Mark where leukocytes are.
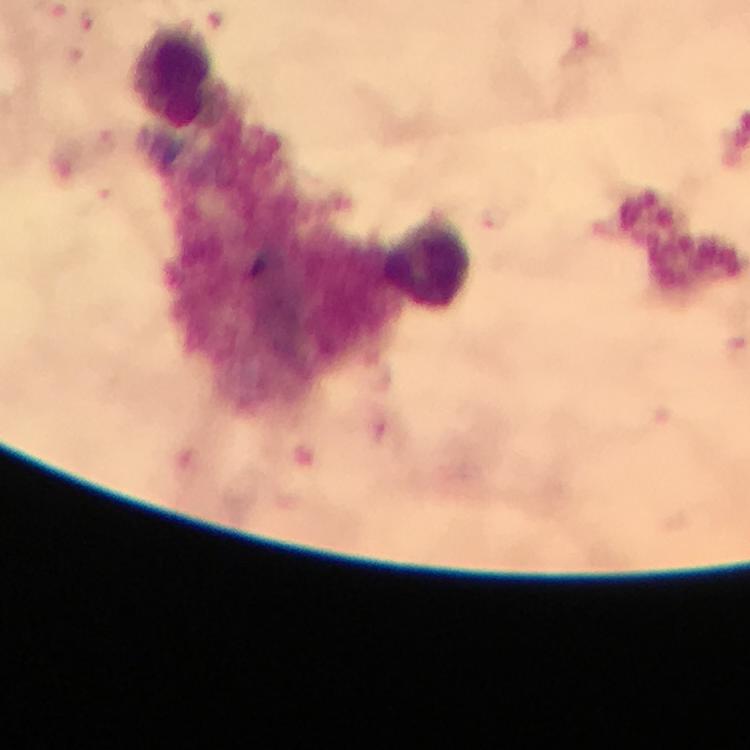

Approximate object centers, in pixels from the top-left corner.
Leukocytes: (x=171, y=74), (x=427, y=261).

Malaria parasite locations: (x=89, y=19), (x=107, y=145), (x=492, y=219). Immersion oil applied. Image is 750×750 pixels. Giemsa-stained preparation. From a malaria diagnostic workup. Thick blood smear. A crop from one field of view. Smartphone photograph taken through a microscope. At 100x magnification.